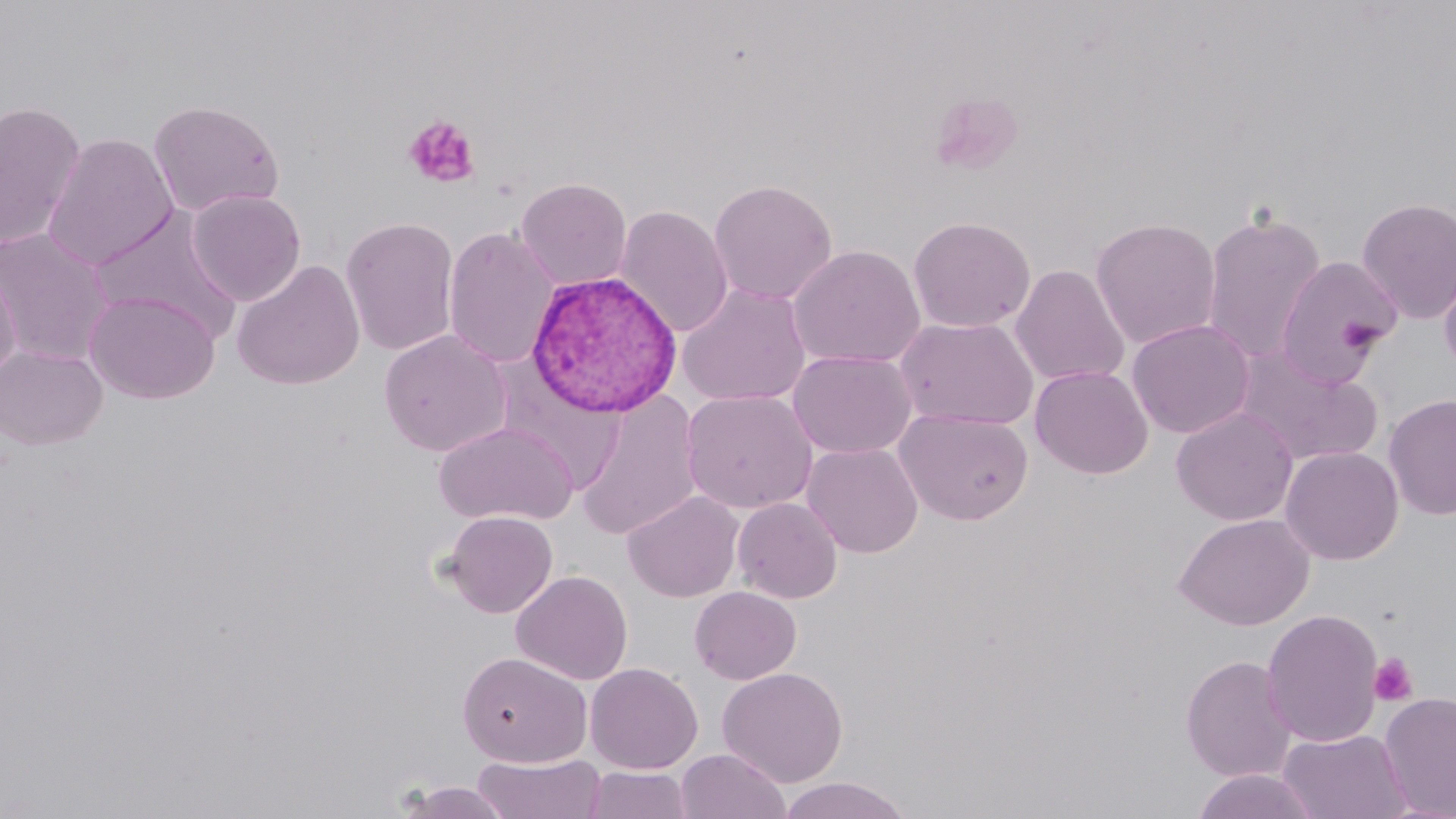
Approximate bounding boxes as (x1, y1, x2, y2) in pixels. Platelet locations (subset): (403, 115, 481, 188), (1340, 315, 1384, 354), (1368, 654, 1418, 706). Uninfected red blood cell locations (subset): (148, 99, 285, 217), (0, 101, 86, 250), (42, 132, 178, 271), (516, 177, 632, 289), (709, 179, 838, 305), (187, 189, 306, 305), (1355, 196, 1456, 325), (615, 205, 734, 338), (88, 206, 243, 341), (1201, 209, 1327, 364), (341, 216, 460, 357), (908, 216, 1036, 333), (1090, 217, 1222, 349), (443, 226, 560, 369), (0, 227, 113, 365), (787, 244, 925, 369), (1274, 254, 1401, 386), (1438, 254, 1456, 380), (232, 259, 365, 391), (1010, 264, 1130, 387), (0, 266, 21, 381), (676, 283, 812, 407), (85, 290, 220, 403), (895, 316, 1038, 430), (1126, 319, 1255, 438), (379, 329, 512, 456), (0, 345, 107, 450), (1233, 345, 1383, 467), (788, 349, 916, 459), (1030, 365, 1153, 479), (681, 389, 818, 514), (576, 391, 703, 541), (1383, 394, 1456, 521), (1171, 406, 1298, 526), (895, 408, 1033, 525), (434, 420, 577, 525), (803, 442, 923, 558), (1280, 445, 1404, 565), (622, 490, 744, 603), (732, 497, 843, 603), (442, 511, 558, 618), (1173, 513, 1314, 631), (511, 570, 632, 685), (689, 586, 801, 684), (1261, 608, 1384, 748), (458, 651, 592, 766), (1181, 654, 1296, 782), (585, 663, 703, 774), (717, 667, 848, 788), (1379, 691, 1456, 818), (1279, 727, 1410, 819), (676, 748, 790, 819), (472, 753, 607, 818), (583, 766, 693, 818), (1191, 769, 1322, 819), (778, 777, 911, 819), (394, 781, 514, 819). Plasmodium vivax-infected red blood cell locations: (526, 270, 683, 418). Slide-level diagnosis: Plasmodium vivax. Optical microscopy. May-Grünwald-Giemsa stain. Image is 1456×819 pixels. One field of a larger specimen. 1000x magnification. Thin blood smear.